State the blood parasite species.
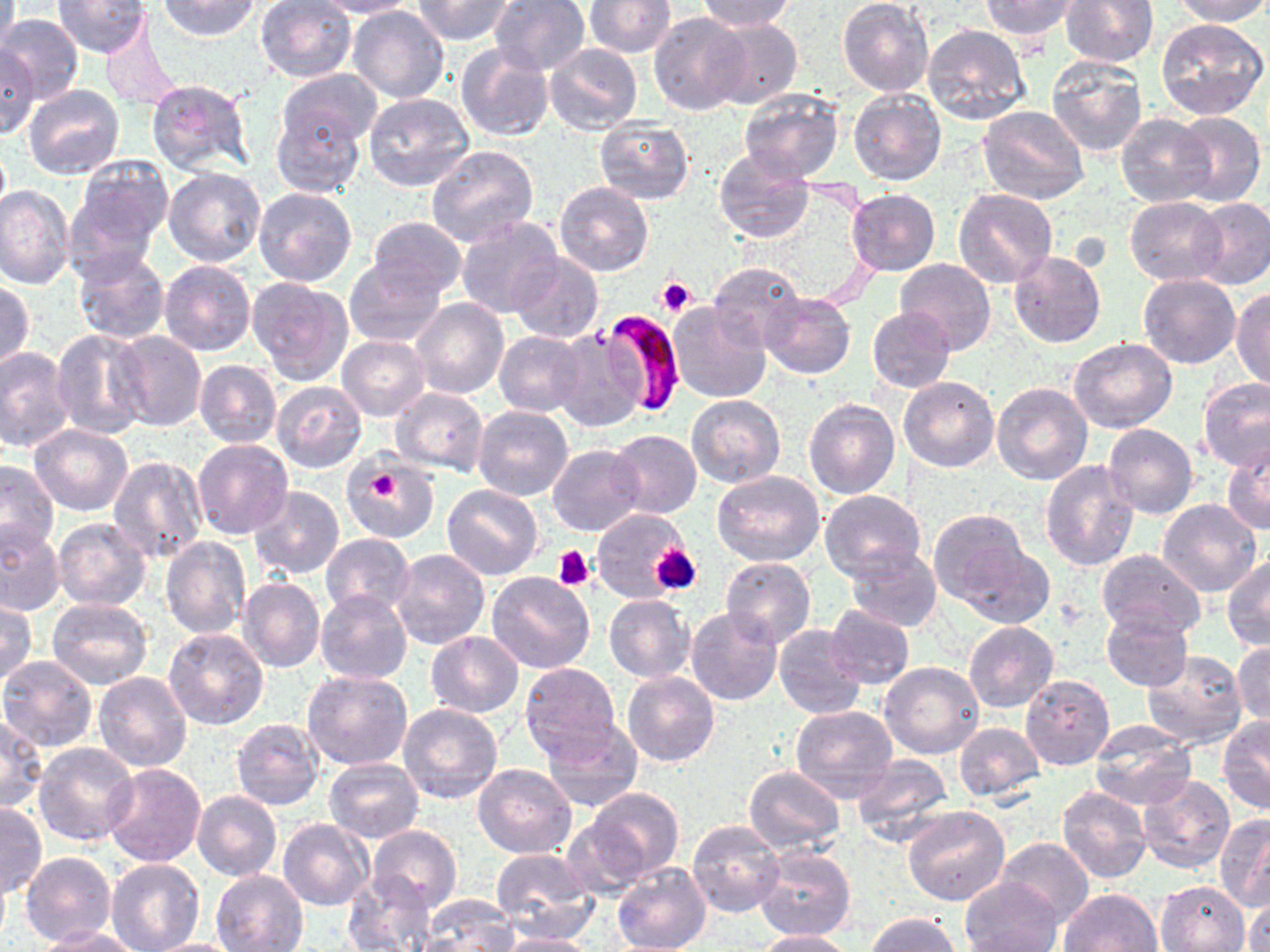
Plasmodium falciparum.

platelet locations = approximate bounding boxes as [x1, y1, x2, y2] in pixels: [658, 277, 696, 317], [361, 463, 410, 509], [651, 544, 701, 595], [556, 546, 593, 589]
stain = May-Grünwald-Giemsa
preparation = thin blood film
uninfected red blood cell locations = approximate bounding boxes as [x1, y1, x2, y2] in pixels: [0, 0, 19, 70], [52, 0, 152, 57], [155, 0, 263, 40], [316, 0, 420, 18], [413, 0, 514, 45], [490, 0, 590, 75], [585, 0, 675, 57], [697, 0, 797, 32], [838, 0, 933, 96], [979, 0, 1081, 41], [1060, 0, 1159, 67], [1169, 0, 1270, 25], [255, 1, 358, 83], [347, 5, 451, 103], [647, 11, 751, 115], [0, 13, 84, 103], [1156, 17, 1269, 121], [707, 18, 802, 110], [98, 21, 181, 110], [922, 23, 1031, 124], [457, 43, 554, 142], [543, 43, 643, 136], [0, 45, 39, 140], [1045, 54, 1150, 156], [278, 69, 382, 150], [145, 78, 254, 175], [22, 85, 125, 180], [738, 88, 843, 183], [847, 89, 945, 186], [362, 93, 475, 192], [979, 104, 1090, 205], [270, 107, 366, 198], [1170, 111, 1265, 206], [1116, 113, 1214, 208], [594, 117, 695, 204], [426, 144, 540, 249], [714, 148, 814, 243], [68, 155, 173, 266], [164, 165, 266, 266], [555, 181, 654, 277], [0, 184, 74, 288], [253, 187, 357, 287], [846, 189, 939, 276], [955, 189, 1058, 290], [1125, 196, 1227, 286], [1191, 198, 1270, 289], [367, 216, 468, 298], [456, 216, 562, 318], [73, 248, 171, 345], [1009, 251, 1106, 348], [508, 252, 604, 343], [896, 258, 996, 355], [159, 259, 256, 355], [344, 259, 446, 347], [708, 262, 803, 350], [1138, 274, 1240, 369], [248, 277, 354, 385], [1, 280, 35, 369], [1231, 287, 1270, 390], [760, 291, 856, 379], [411, 298, 509, 399], [668, 302, 769, 402], [867, 305, 955, 393], [549, 326, 648, 432], [50, 328, 152, 440], [494, 330, 587, 417], [111, 331, 205, 431], [337, 336, 430, 420], [1068, 337, 1176, 433], [0, 348, 74, 455], [195, 359, 283, 449], [1198, 376, 1270, 471], [898, 377, 998, 472], [272, 380, 366, 472], [992, 382, 1093, 485], [391, 389, 489, 475], [687, 393, 785, 488], [804, 399, 901, 500], [473, 405, 574, 501], [29, 424, 134, 516], [1103, 424, 1197, 519], [607, 429, 701, 518], [192, 438, 293, 539], [1223, 443, 1270, 533], [547, 444, 645, 536], [108, 452, 208, 564], [343, 456, 440, 543], [1040, 459, 1139, 571], [0, 460, 58, 556], [712, 470, 825, 567], [442, 484, 544, 580], [249, 486, 345, 579], [819, 490, 927, 582], [1157, 501, 1262, 597], [590, 507, 690, 604], [928, 510, 1030, 607], [52, 517, 152, 610], [0, 524, 64, 616], [322, 533, 414, 617], [160, 536, 251, 640], [958, 541, 1053, 628], [844, 547, 942, 631], [388, 548, 489, 649], [1096, 549, 1204, 637], [1222, 554, 1270, 651], [720, 557, 816, 648], [486, 571, 596, 674], [239, 577, 324, 672], [317, 589, 411, 684], [604, 595, 695, 681], [47, 598, 154, 691], [0, 600, 38, 687], [825, 605, 915, 689], [687, 607, 782, 705], [1101, 609, 1192, 691], [964, 622, 1058, 712], [773, 623, 866, 719], [162, 626, 269, 729], [424, 631, 523, 717], [1231, 641, 1270, 726], [1141, 651, 1248, 749], [0, 655, 100, 751], [880, 661, 983, 758], [519, 662, 621, 760], [302, 668, 414, 771], [93, 672, 193, 772], [623, 672, 718, 767], [1021, 674, 1115, 771], [399, 704, 502, 804], [790, 704, 900, 804], [0, 716, 47, 814], [540, 717, 643, 813], [1219, 717, 1270, 814], [232, 718, 325, 812], [954, 722, 1044, 801], [1088, 722, 1195, 810], [33, 742, 139, 847], [851, 754, 953, 848], [326, 758, 423, 842], [102, 763, 206, 868], [473, 763, 576, 858], [744, 766, 845, 853], [1133, 773, 1236, 873], [580, 786, 686, 883], [1057, 786, 1151, 883], [192, 791, 282, 882], [0, 801, 45, 899], [902, 805, 1010, 906], [1214, 814, 1270, 911], [278, 818, 371, 910], [687, 819, 784, 917], [369, 825, 462, 913], [994, 837, 1093, 928], [752, 846, 855, 941], [490, 847, 599, 935], [21, 851, 116, 947], [106, 860, 204, 952], [612, 864, 711, 952], [211, 870, 309, 951], [345, 874, 434, 951], [959, 877, 1062, 952], [1154, 880, 1249, 952], [1057, 888, 1162, 952], [1243, 893, 1269, 951], [416, 896, 518, 952], [868, 913, 963, 952], [38, 926, 141, 951], [753, 929, 853, 951], [496, 932, 601, 952], [142, 937, 250, 952]
image size = 1270×952 pixels
field of view = single
modality = optical microscopy
magnification = 1000x
Plasmodium falciparum-infected red blood cell locations = approximate bounding boxes as [x1, y1, x2, y2] in pixels: [600, 306, 690, 416]